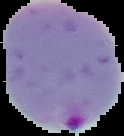

From a thin blood smear. Result: malaria parasites detected. Segmented cell region on a black background. Image is 124×136 pixels.